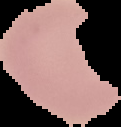
Summary:
  - Preparation: thin blood smear
  - Result: no malaria parasites detected
  - Image type: segmented cell region with the area outside set to black
  - Image size: 121×127 pixels